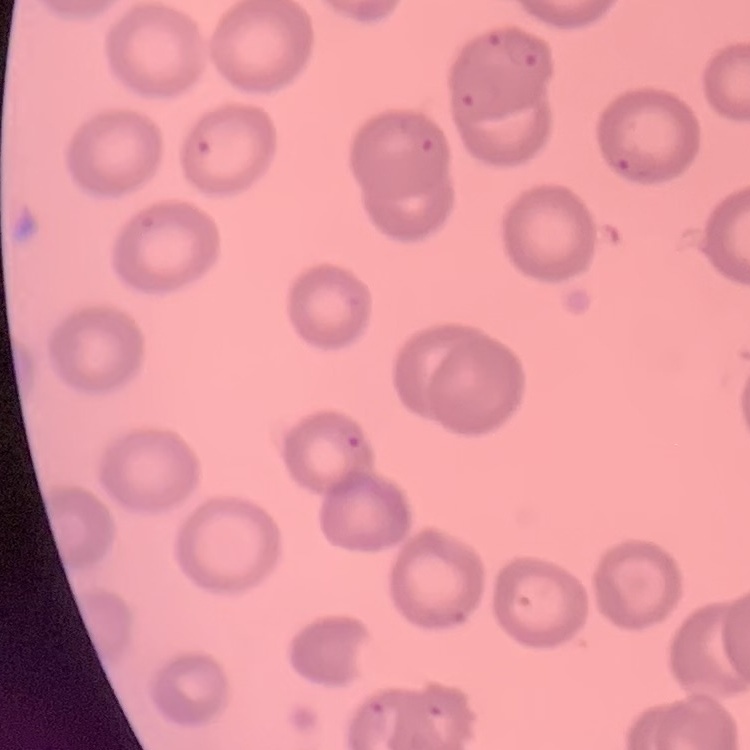

red_blood_cell_morphology: no rouleaux formation
image_type: one tile cut from a larger photomicrograph
stain: Field's or Giemsa
preparation: thin blood smear